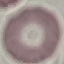

Malaria status: uninfected. Giemsa-stained preparation. Thin blood film. Photographed with a smartphone camera at the microscope eyepiece. Cell patch, automatically extracted from a larger field of view and resized to 64 × 64 pixels.